Give the extent of all uninfected red blood cells.
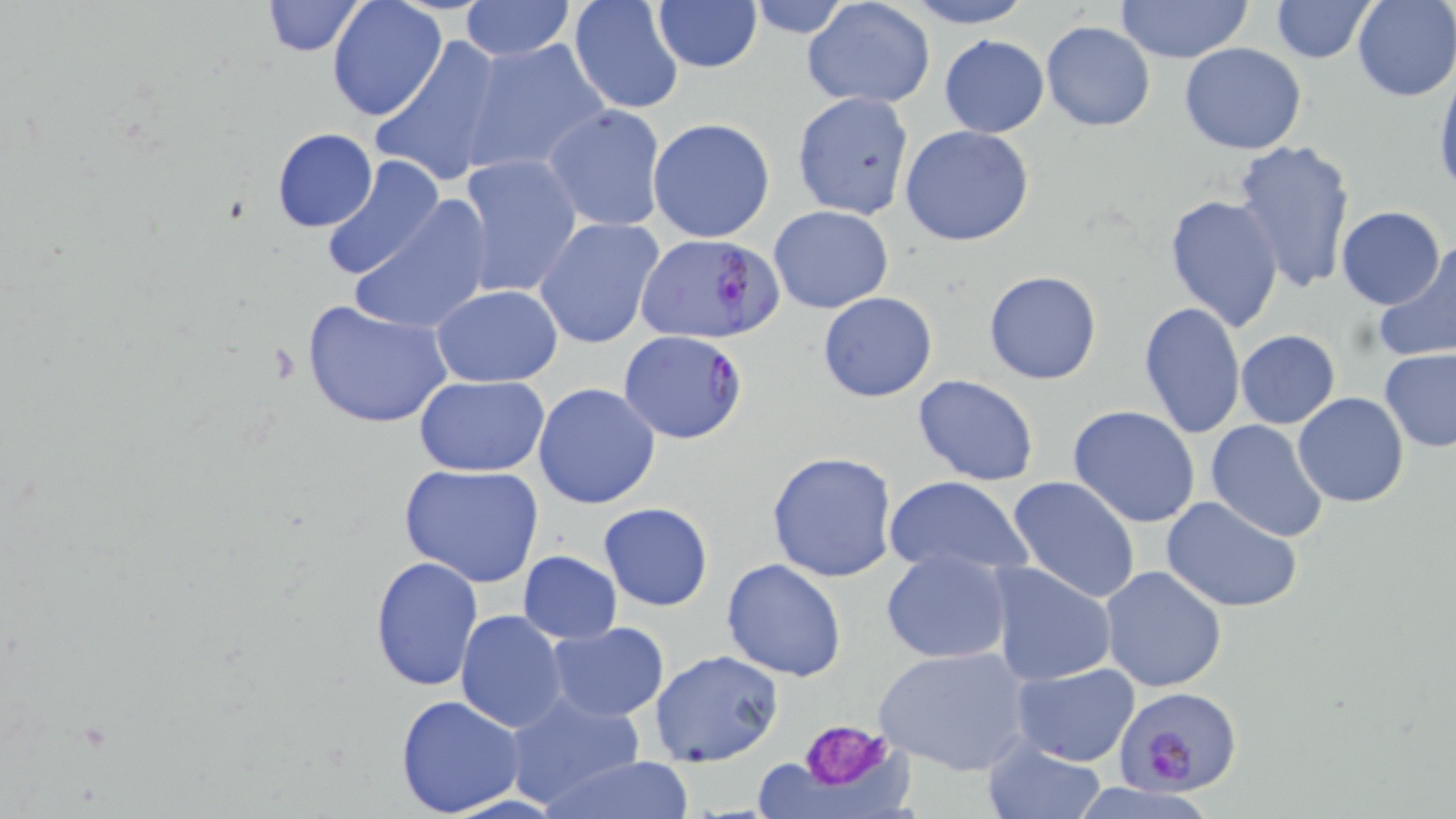

Approximate bounding boxes as (x1, y1, x2, y2) in pixels.
Uninfected red blood cells: (257, 0, 366, 56), (568, 0, 686, 116), (801, 0, 935, 109), (901, 0, 1036, 28), (1114, 0, 1254, 63), (1352, 0, 1456, 101), (327, 1, 447, 120), (459, 1, 574, 61), (650, 1, 762, 72), (743, 1, 859, 38), (1270, 1, 1375, 64), (1042, 20, 1155, 131), (938, 35, 1050, 138), (370, 37, 506, 187), (463, 39, 612, 175), (1178, 43, 1307, 154), (1433, 71, 1456, 199), (791, 92, 916, 218), (543, 104, 667, 233), (791, 110, 1035, 233), (648, 117, 777, 243), (900, 126, 1034, 246), (270, 128, 378, 232), (1231, 137, 1357, 296), (456, 154, 583, 300), (319, 155, 446, 282), (1163, 194, 1285, 333), (350, 196, 495, 335), (769, 205, 893, 313), (1336, 206, 1444, 309), (535, 217, 665, 349), (1373, 237, 1456, 366), (983, 270, 1103, 385), (432, 285, 562, 385), (817, 292, 937, 403), (303, 299, 453, 430), (1137, 299, 1245, 438), (1235, 330, 1340, 429), (1378, 348, 1456, 452), (414, 375, 551, 474), (912, 375, 1040, 488), (533, 383, 660, 508), (1293, 393, 1408, 509), (1067, 406, 1201, 530), (1205, 418, 1329, 541), (766, 450, 898, 582), (399, 463, 546, 588), (883, 474, 1032, 579), (1007, 475, 1142, 605), (1161, 495, 1303, 612), (598, 501, 713, 612), (518, 550, 621, 643), (881, 550, 1012, 664), (369, 555, 482, 691), (722, 558, 849, 680), (985, 561, 1118, 687), (1098, 565, 1227, 693), (456, 611, 569, 732), (545, 622, 670, 721), (875, 643, 1035, 776), (650, 648, 784, 767), (1011, 663, 1140, 766), (501, 688, 649, 809), (393, 695, 527, 817), (983, 741, 1104, 818), (540, 755, 697, 819), (752, 760, 836, 817).

Platelet locations: (798, 716, 894, 788). Plasmodium falciparum-infected red blood cell locations: (635, 232, 785, 345), (618, 331, 749, 444), (1117, 688, 1241, 796). Slide-level diagnosis: Plasmodium falciparum. May-Grünwald-Giemsa stain. Captured at 1000x magnification. Optical microscopy. One field of a larger specimen. Image is 1456×819 pixels. Thin blood smear.